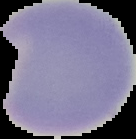 Image is 136×139 pixels. Segmented cell region on a black background. Result: no Plasmodium parasites seen. From a thin blood film.